Outline each Babesia divergens-infected red blood cell.
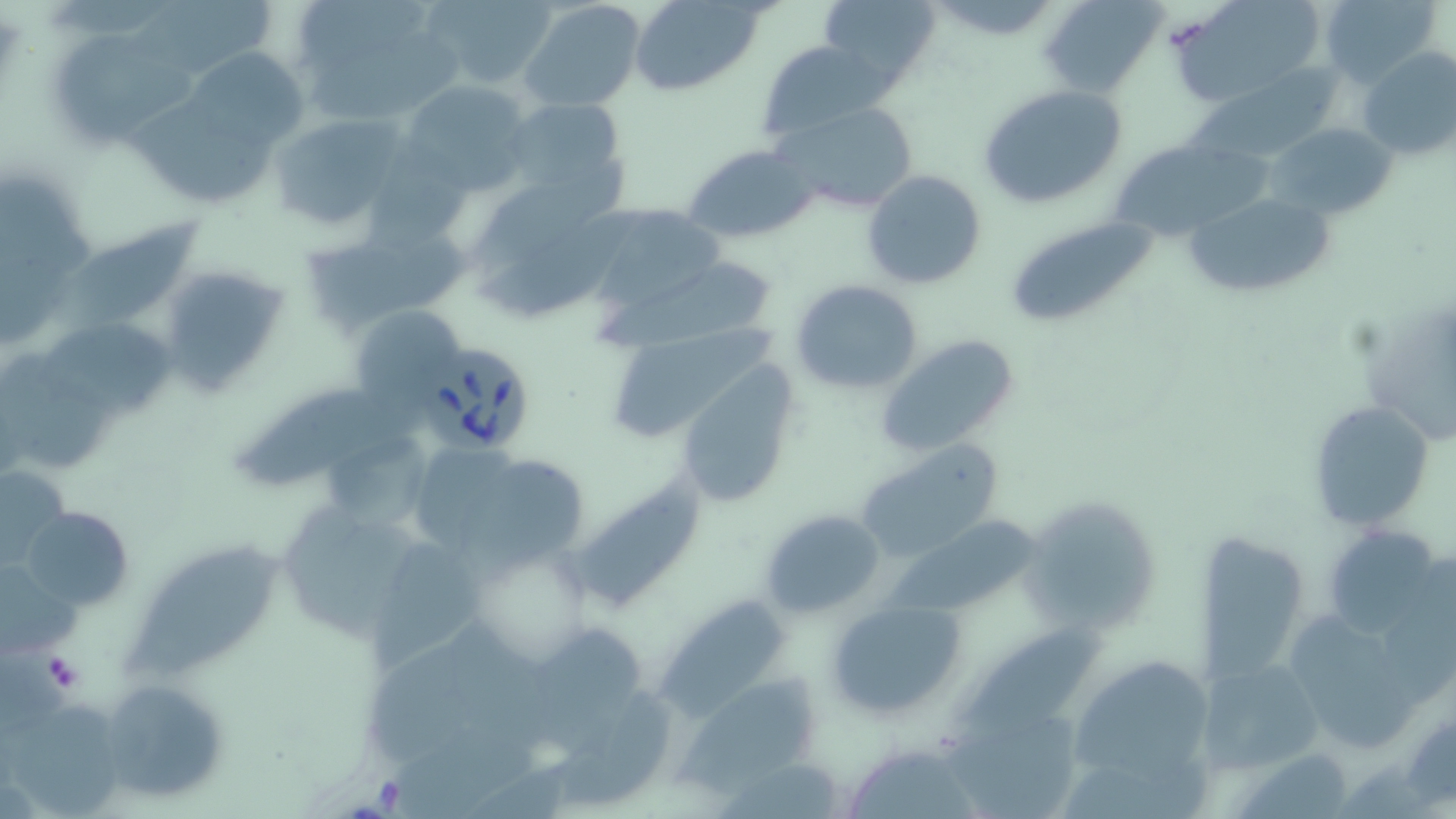
Approximate bounding boxes as named x1/y1/x2/y2 corners in pixels.
Babesia divergens-infected red blood cells: (x1=417, y1=339, x2=536, y2=458).

{
  "slide_level_diagnosis": "Babesia divergens",
  "stain": "May-Grünwald-Giemsa",
  "platelet_locations": "approximate bounding boxes as named x1/y1/x2/y2 corners in pixels: (x1=42, y1=651, x2=86, y2=693)",
  "image_size": "1456×819 pixels",
  "preparation": "thin blood film",
  "uninfected_red_blood_cell_locations": "approximate bounding boxes as named x1/y1/x2/y2 corners in pixels: (x1=421, y1=0, x2=558, y2=89), (x1=519, y1=0, x2=647, y2=112), (x1=629, y1=0, x2=767, y2=96), (x1=818, y1=0, x2=942, y2=93), (x1=1040, y1=0, x2=1166, y2=98), (x1=1175, y1=0, x2=1326, y2=107), (x1=1316, y1=0, x2=1444, y2=88), (x1=122, y1=1, x2=286, y2=80), (x1=295, y1=5, x2=432, y2=70), (x1=54, y1=33, x2=205, y2=143), (x1=757, y1=40, x2=894, y2=141), (x1=300, y1=41, x2=469, y2=125), (x1=1357, y1=47, x2=1455, y2=161), (x1=181, y1=49, x2=305, y2=151), (x1=1184, y1=60, x2=1346, y2=158), (x1=399, y1=80, x2=530, y2=194), (x1=977, y1=85, x2=1129, y2=211), (x1=121, y1=88, x2=279, y2=209), (x1=497, y1=96, x2=629, y2=212), (x1=772, y1=101, x2=921, y2=217), (x1=267, y1=113, x2=407, y2=231), (x1=1267, y1=122, x2=1395, y2=220), (x1=1113, y1=142, x2=1278, y2=240), (x1=684, y1=143, x2=820, y2=243), (x1=862, y1=168, x2=987, y2=290), (x1=462, y1=178, x2=621, y2=326), (x1=1185, y1=192, x2=1335, y2=300), (x1=578, y1=204, x2=721, y2=313), (x1=1007, y1=217, x2=1162, y2=328), (x1=65, y1=221, x2=201, y2=329), (x1=302, y1=221, x2=479, y2=339), (x1=593, y1=253, x2=780, y2=354), (x1=155, y1=263, x2=295, y2=396), (x1=790, y1=279, x2=922, y2=394), (x1=347, y1=305, x2=469, y2=411), (x1=44, y1=306, x2=186, y2=418), (x1=605, y1=320, x2=791, y2=453), (x1=873, y1=334, x2=1023, y2=458), (x1=678, y1=369, x2=800, y2=509), (x1=233, y1=381, x2=408, y2=496), (x1=1307, y1=397, x2=1432, y2=533), (x1=857, y1=439, x2=1002, y2=559), (x1=460, y1=457, x2=593, y2=583), (x1=1, y1=466, x2=70, y2=567), (x1=570, y1=472, x2=705, y2=607), (x1=1020, y1=500, x2=1150, y2=638), (x1=279, y1=504, x2=433, y2=641), (x1=881, y1=504, x2=1035, y2=615), (x1=21, y1=505, x2=134, y2=610), (x1=760, y1=508, x2=887, y2=619), (x1=1320, y1=523, x2=1448, y2=640), (x1=1200, y1=532, x2=1307, y2=692), (x1=123, y1=540, x2=295, y2=690), (x1=369, y1=542, x2=496, y2=676), (x1=652, y1=595, x2=788, y2=724), (x1=828, y1=599, x2=965, y2=719), (x1=1292, y1=617, x2=1420, y2=751), (x1=956, y1=619, x2=1113, y2=736), (x1=515, y1=622, x2=658, y2=761), (x1=1195, y1=652, x2=1327, y2=781), (x1=1071, y1=654, x2=1209, y2=780), (x1=99, y1=677, x2=229, y2=805), (x1=664, y1=677, x2=819, y2=814), (x1=3, y1=700, x2=122, y2=815), (x1=937, y1=712, x2=1098, y2=819), (x1=853, y1=745, x2=975, y2=819)",
  "modality": "light microscopy",
  "field_of_view": "single",
  "magnification": "1000x"
}